Give the extent of all Plasmodium falciparum-infected red blood cells.
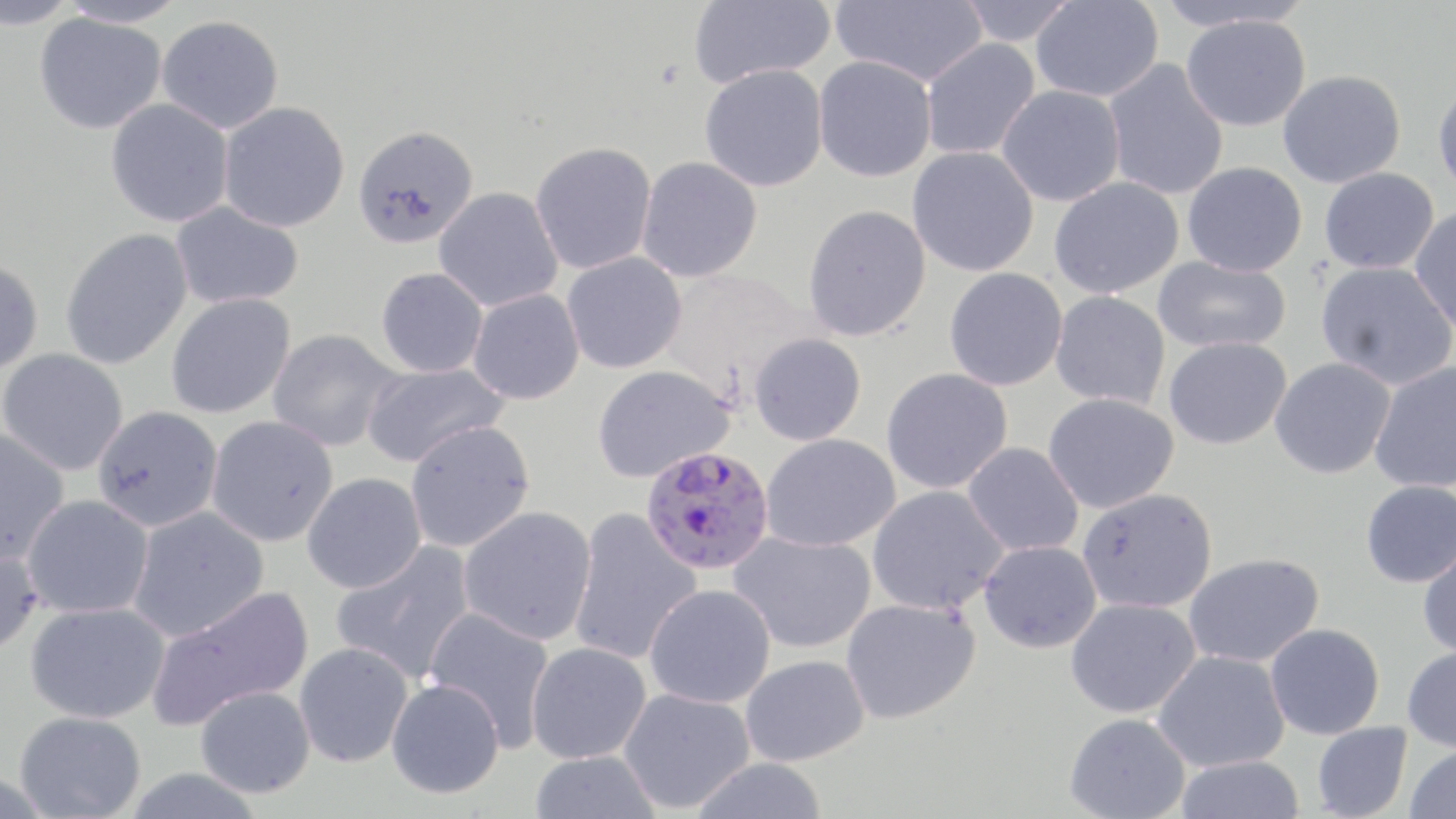
Approximate bounding boxes as (x1,y1)-(x2,y2) corner pairs in pixels.
Plasmodium falciparum-infected red blood cells: (640,445)-(774,575).

slide-level diagnosis = Plasmodium falciparum
field of view = one of a larger specimen
uninfected red blood cell locations = approximate bounding boxes as (x1,y1)-(x2,y2) corner pairs in pixels: (0,0)-(79,29), (57,0)-(188,29), (688,0)-(835,88), (831,0)-(988,88), (957,0)-(1079,46), (1150,0)-(1314,32), (1030,1)-(1163,103), (34,12)-(166,134), (1181,14)-(1311,132), (157,15)-(283,134), (920,39)-(1040,159), (813,56)-(936,182), (1103,59)-(1229,201), (699,64)-(828,192), (1278,70)-(1406,188), (1433,78)-(1456,198), (998,85)-(1125,207), (105,98)-(234,227), (218,101)-(351,232), (352,125)-(478,248), (530,141)-(657,274), (907,146)-(1039,277), (636,156)-(763,282), (1182,162)-(1307,277), (1318,168)-(1439,274), (1048,177)-(1184,299), (434,187)-(564,311), (171,202)-(303,309), (802,204)-(932,341), (1410,206)-(1456,335), (60,228)-(193,370), (562,252)-(687,373), (1153,256)-(1291,355), (0,258)-(44,374), (1315,261)-(1455,390), (376,267)-(488,377), (944,267)-(1067,390), (468,289)-(585,405), (1050,291)-(1170,410), (166,293)-(296,418), (267,329)-(402,452), (749,333)-(866,446), (1163,336)-(1292,450), (0,349)-(129,476), (1269,357)-(1396,479), (360,362)-(510,467), (1368,362)-(1456,494), (592,364)-(734,483), (881,368)-(1013,494), (1042,392)-(1179,513), (91,406)-(223,532), (206,416)-(338,547), (404,421)-(535,553), (0,428)-(69,565), (760,434)-(900,552), (963,442)-(1084,557), (302,472)-(427,594), (1360,481)-(1456,587), (867,485)-(1008,615), (1077,488)-(1217,614), (21,495)-(154,619), (458,506)-(597,646), (128,507)-(269,641), (567,509)-(703,665), (729,531)-(876,653), (979,540)-(1101,652), (0,542)-(43,657), (330,542)-(477,685), (1417,542)-(1456,660), (1183,553)-(1324,668), (644,584)-(775,708), (146,585)-(315,729), (1065,597)-(1201,718), (841,598)-(980,724), (24,601)-(170,723), (423,607)-(555,748), (1265,623)-(1385,740), (295,642)-(413,767), (526,642)-(651,764), (1401,645)-(1456,752), (1152,650)-(1290,773), (740,655)-(870,766), (386,679)-(504,799), (195,685)-(315,798), (618,688)-(755,814), (14,711)-(146,819), (1064,713)-(1191,819), (1312,722)-(1413,819), (1404,744)-(1456,819), (530,751)-(661,819), (1175,755)-(1305,819), (688,757)-(831,819), (122,767)-(264,819), (0,770)-(54,819)
image size = 1456×819 pixels
modality = optical microscopy
preparation = thin blood smear
stain = May-Grünwald-Giemsa
magnification = 1000x